Report the malaria status of this cell.
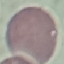
Uninfected.

image type = automatically extracted cell patch, resized to 64 × 64 pixels
capture = smartphone through the microscope eyepiece
stain = Giemsa
preparation = thin smear